Report the malaria status of this cell.
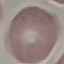

It is uninfected.

Summary:
  - Image type: cell patch, automatically extracted from a larger field of view and resized to 64 × 64 pixels
  - Preparation: thin blood smear
  - Stain: Giemsa
  - Capture: smartphone camera at the microscope eyepiece